Give the extent of all Plasmodium falciparum-infected red blood cells.
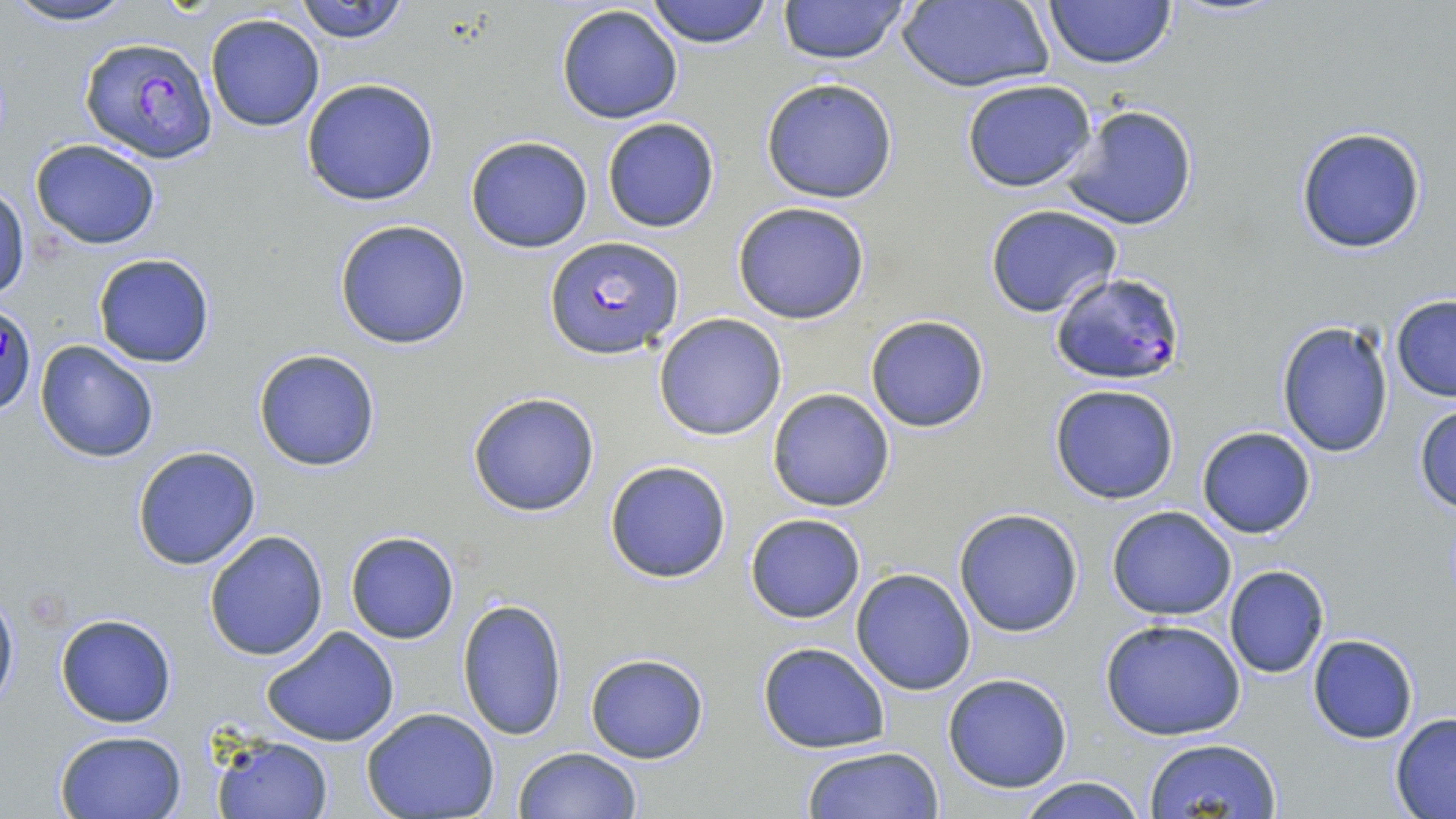

Approximate bounding boxes as [x1, y1, x2, y2] in pixels.
Plasmodium falciparum-infected red blood cells: [80, 36, 217, 162], [545, 236, 682, 358], [1048, 273, 1185, 385], [2, 306, 37, 417].

{
  "slide_level_diagnosis": "Plasmodium falciparum",
  "preparation": "thin blood film",
  "field_of_view": "one of a larger specimen",
  "modality": "light microscopy",
  "image_size": "1456×819 pixels",
  "magnification": "1000x",
  "stain": "May-Grünwald-Giemsa",
  "uninfected_red_blood_cell_locations": "approximate bounding boxes as [x1, y1, x2, y2] in pixels: [5, 0, 138, 26], [645, 0, 773, 48], [774, 0, 913, 66], [1043, 0, 1175, 69], [294, 1, 413, 45], [897, 1, 1054, 92], [556, 5, 683, 124], [206, 14, 324, 132], [299, 78, 441, 206], [760, 78, 900, 204], [959, 79, 1099, 191], [1059, 103, 1199, 232], [601, 117, 720, 233], [1293, 126, 1427, 254], [464, 135, 593, 253], [30, 139, 161, 250], [1, 185, 29, 301], [731, 200, 870, 325], [984, 204, 1124, 318], [333, 219, 472, 350], [91, 252, 217, 369], [1390, 295, 1456, 402], [654, 313, 787, 441], [864, 314, 990, 432], [1276, 319, 1396, 457], [35, 341, 159, 464], [253, 347, 382, 472], [1049, 383, 1181, 504], [767, 388, 897, 512], [466, 390, 602, 517], [1412, 402, 1456, 514], [1195, 425, 1317, 538], [131, 446, 261, 571], [604, 459, 731, 583], [1106, 505, 1238, 620], [952, 508, 1084, 637], [744, 512, 867, 624], [203, 530, 329, 661], [345, 532, 460, 644], [1224, 566, 1331, 679], [850, 567, 978, 695], [0, 582, 19, 715], [455, 598, 569, 742], [55, 612, 178, 728], [1099, 617, 1245, 741], [261, 626, 400, 747], [1307, 635, 1419, 744], [756, 641, 889, 752], [584, 650, 710, 765], [943, 674, 1073, 792], [360, 709, 500, 819], [1390, 712, 1456, 817], [54, 729, 188, 819], [212, 733, 333, 818], [1148, 737, 1279, 818], [799, 745, 946, 819], [511, 747, 642, 819], [1014, 776, 1147, 818]"
}